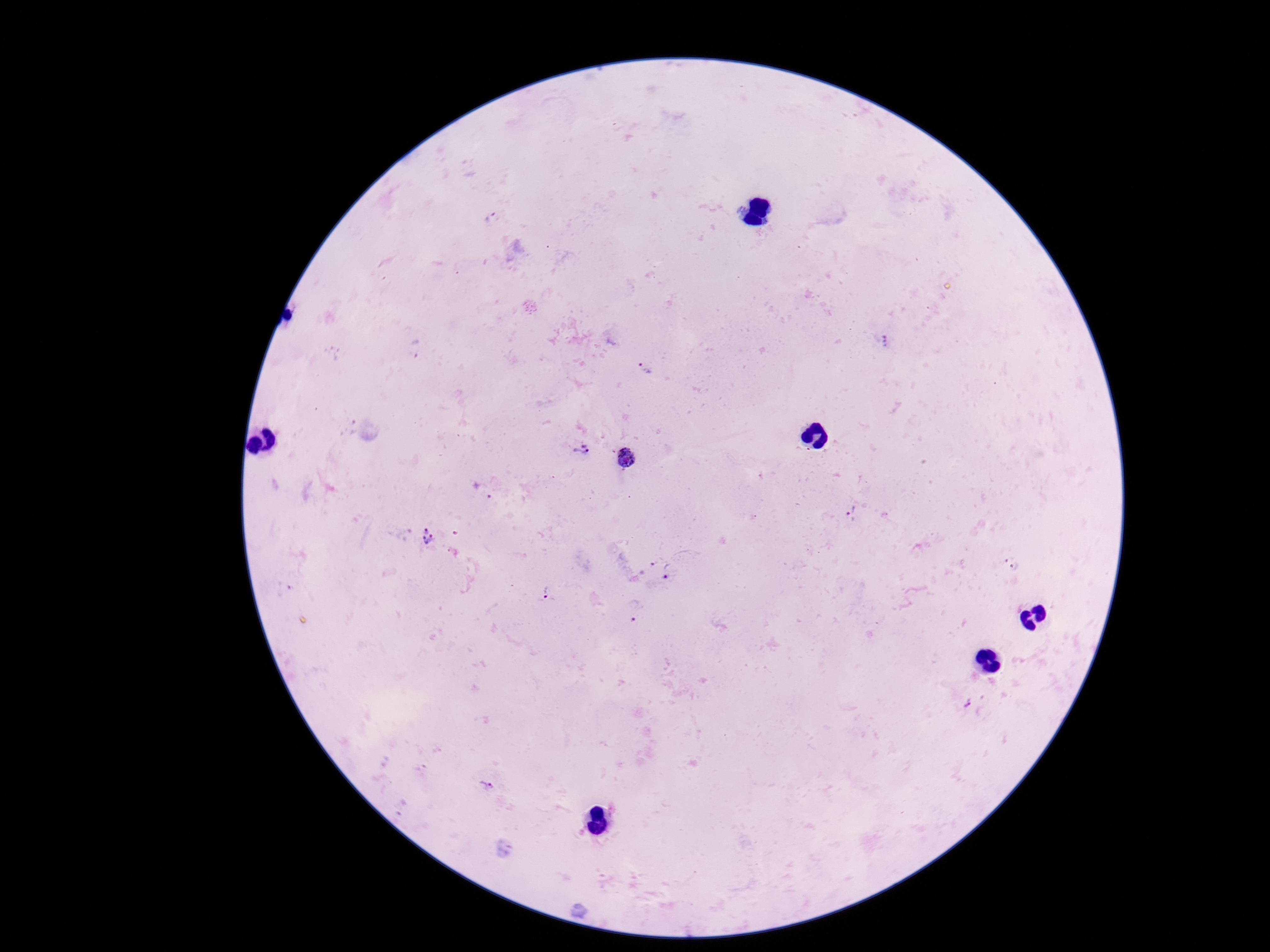

stain: Giemsa
plasmodium_parasite_locations: 'approximate centers as {x, y} in pixels: {491, 217}, {883, 339}, {416, 348}, {645, 368}, {578, 451}, {627, 457}, {482, 492}, {854, 513}, {427, 536}, {645, 566}, {1015, 566}, {671, 570}, {547, 592}, {634, 613}, {967, 705}, {489, 785}'
field_of_view: single
capture: smartphone camera through the microscope eyepiece
image_size: 1270×952 pixels
magnification: 100x
preparation: thick blood film
patient_malaria_status: positive